Point out each Plasmodium parasite.
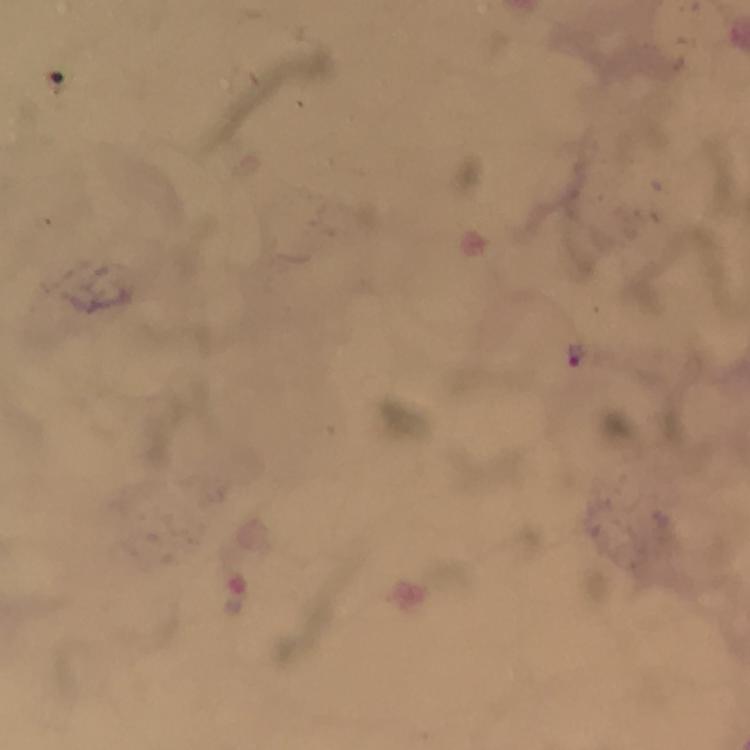
Approximate centers as (x, y) in pixels.
Plasmodium parasites: (576, 355).

context: from a malaria diagnostic workup
cropped_from: one field of view
image_size: 750×750 pixels
immersion_oil: applied
capture: smartphone mounted on the microscope
stain: Giemsa
preparation: thick smear
magnification: 100x